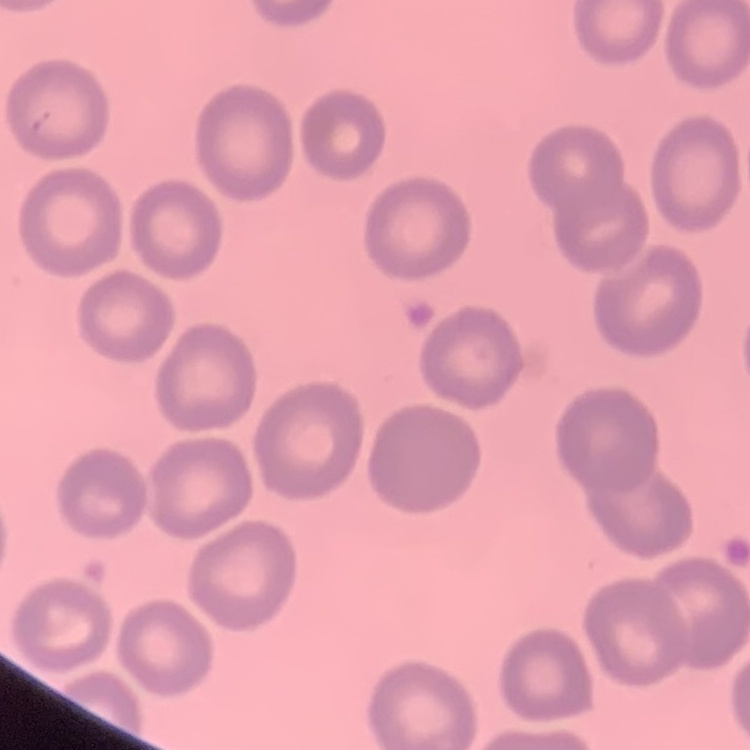

erythrocyte morphology = no rouleaux formation
image type = square crop of a larger photomicrograph
stain = Field's or Giemsa
preparation = thin blood film